State the blood parasite species.
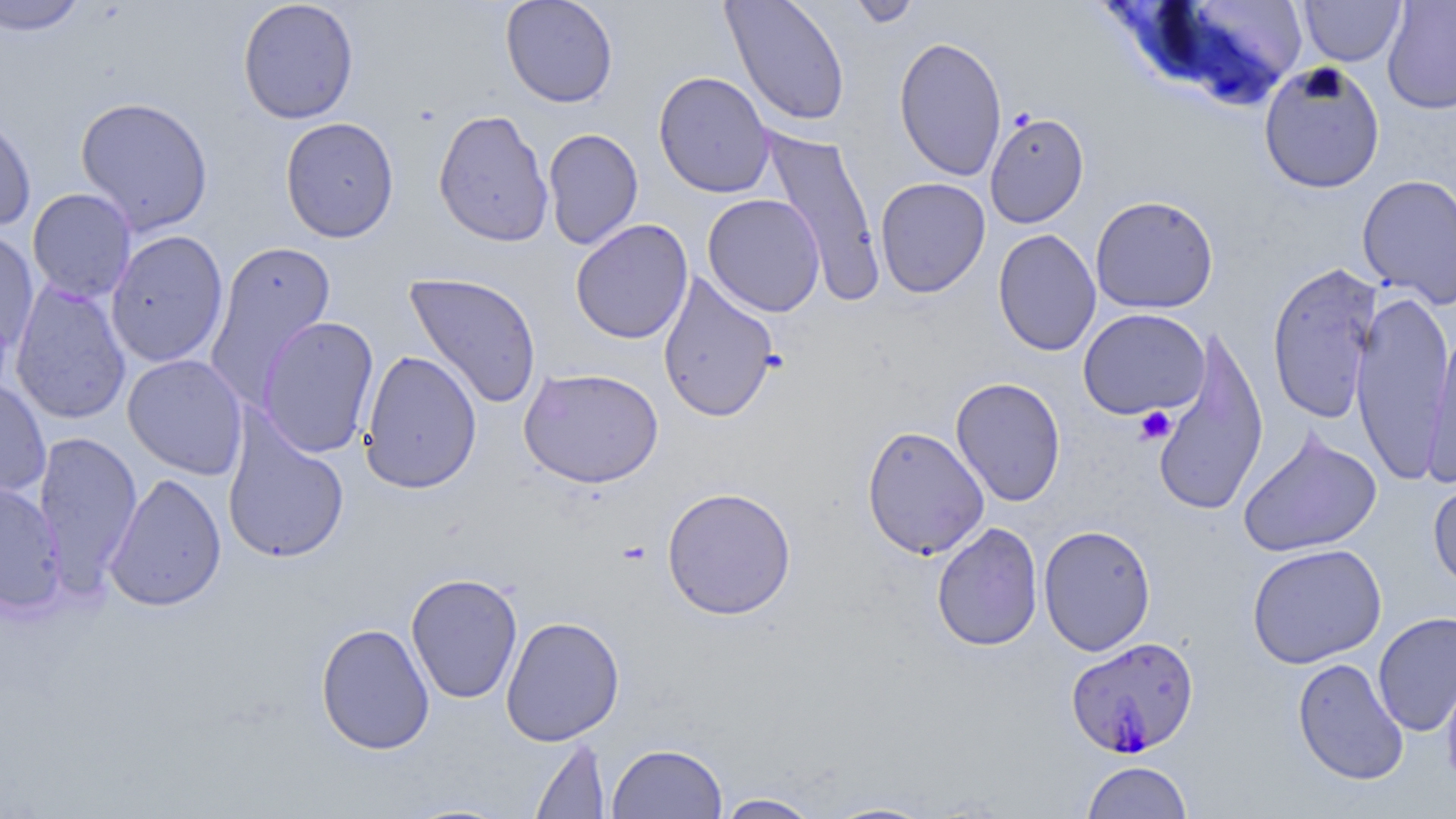

Plasmodium falciparum.

uninfected red blood cell locations = approximate bounding boxes as (x1, y1, x2, y2) in pixels: (0, 0, 89, 35), (238, 0, 360, 124), (500, 0, 619, 108), (721, 0, 851, 127), (846, 0, 923, 28), (1299, 0, 1406, 66), (1382, 0, 1456, 114), (1145, 1, 1309, 109), (894, 35, 1007, 181), (1258, 61, 1385, 194), (653, 71, 775, 198), (74, 96, 214, 236), (433, 108, 554, 247), (0, 109, 37, 232), (985, 111, 1089, 229), (280, 116, 399, 243), (542, 128, 643, 249), (761, 129, 885, 303), (1357, 173, 1456, 308), (875, 177, 991, 298), (27, 188, 137, 304), (702, 193, 826, 317), (1090, 195, 1219, 314), (570, 219, 694, 345), (0, 229, 39, 357), (106, 229, 229, 368), (993, 229, 1101, 356), (204, 240, 336, 404), (1266, 261, 1383, 423), (657, 270, 780, 423), (404, 272, 543, 409), (9, 280, 132, 425), (1350, 291, 1456, 485), (1077, 308, 1210, 419), (256, 316, 380, 458), (1422, 326, 1456, 485), (1150, 329, 1269, 517), (358, 350, 483, 495), (122, 354, 249, 479), (519, 367, 664, 487), (0, 375, 51, 501), (951, 376, 1066, 507), (222, 418, 350, 564), (861, 424, 990, 560), (1237, 427, 1382, 558), (33, 431, 142, 590), (104, 472, 227, 612), (1428, 475, 1456, 593), (0, 481, 67, 614), (661, 486, 797, 620), (931, 522, 1043, 652), (1038, 524, 1156, 656), (1247, 543, 1387, 668), (406, 572, 523, 704), (1372, 611, 1456, 738), (500, 616, 625, 746), (315, 622, 435, 755), (1292, 657, 1409, 785), (1440, 664, 1456, 790), (530, 738, 611, 818), (607, 742, 728, 819), (1081, 760, 1194, 818), (713, 793, 824, 818), (819, 800, 941, 818)
magnification = 1000x
platelet locations = approximate bounding boxes as (x1, y1, x2, y2) in pixels: (1134, 406, 1176, 445)
field of view = one of a larger specimen
preparation = thin blood film
modality = light microscopy
stain = May-Grünwald-Giemsa
Plasmodium falciparum-infected red blood cell locations = approximate bounding boxes as (x1, y1, x2, y2) in pixels: (1066, 636, 1200, 760)
image size = 1456×819 pixels